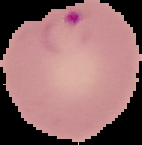 Result: Plasmodium parasites detected. Image is 142×145 pixels. The area outside the segmented cell region is set to black. From a thin blood smear.